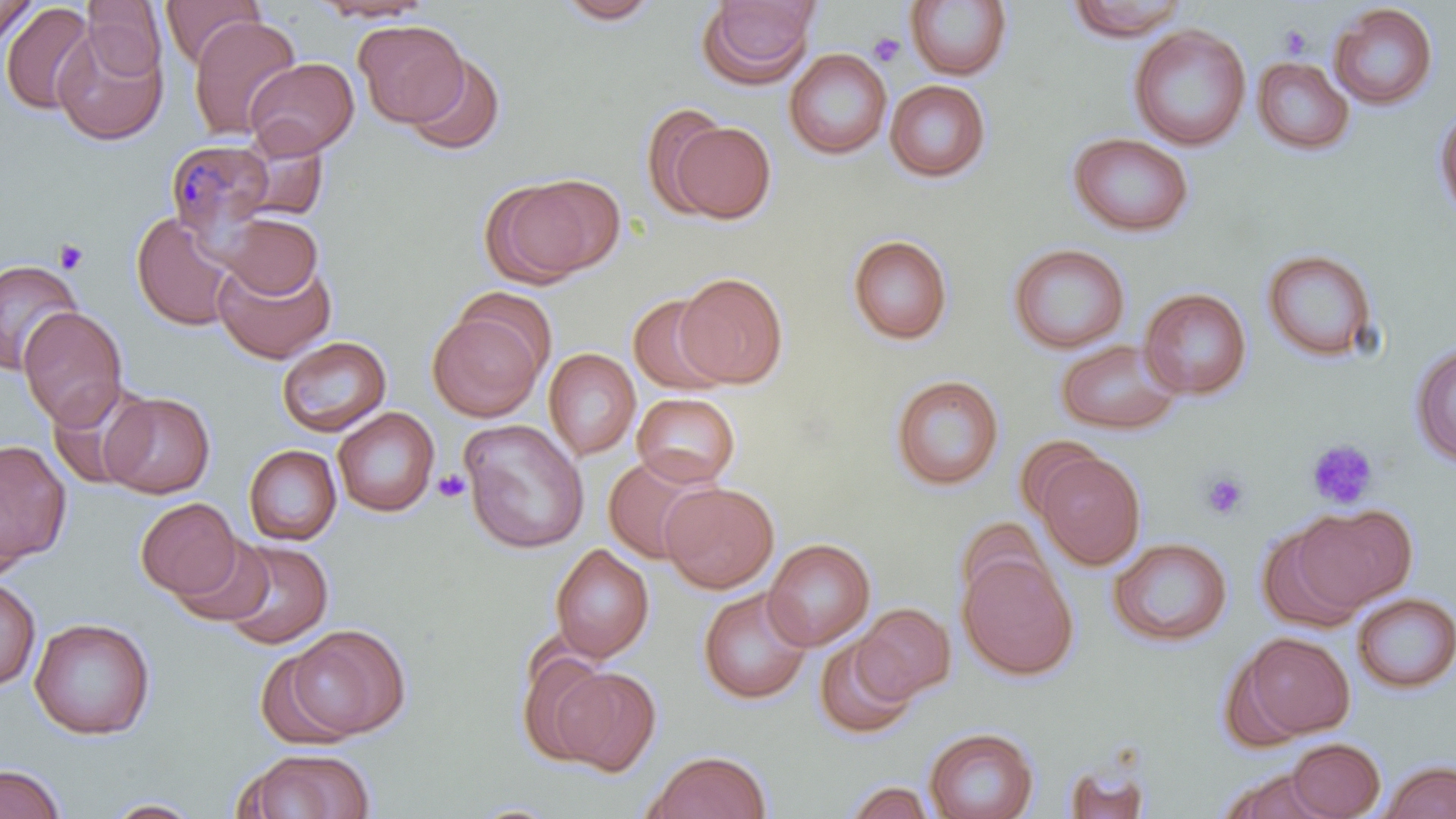
Summary:
  - Coordinate format: approximate bounding boxes as (x1,y1)-(x2,y2) corner pairs in pixels
  - Uninfected red blood cell locations: (82,0)-(167,78), (160,0)-(265,69), (308,0)-(436,23), (554,0)-(663,25), (1065,0)-(1191,42), (0,1)-(37,49), (696,1)-(821,89), (904,1)-(1013,81), (0,3)-(97,115), (1328,3)-(1439,111), (188,15)-(301,140), (354,20)-(468,127), (52,23)-(168,146), (1128,24)-(1251,152), (784,48)-(892,160), (403,51)-(505,156), (245,57)-(360,158), (1252,57)-(1355,156), (885,80)-(992,183), (1433,101)-(1456,225), (641,104)-(732,217), (664,120)-(777,223), (232,131)-(330,223), (1067,132)-(1194,237), (483,175)-(616,285), (131,211)-(239,332), (218,212)-(323,299), (846,234)-(953,345), (1007,242)-(1131,354), (1261,248)-(1380,364), (212,255)-(336,364), (0,259)-(83,374), (675,272)-(788,388), (454,286)-(558,377), (1139,287)-(1252,400), (627,295)-(731,396), (18,306)-(128,429), (428,309)-(544,421), (276,335)-(392,436), (1055,339)-(1183,435), (1408,340)-(1456,467), (543,348)-(641,460), (890,374)-(1005,491), (47,378)-(156,491), (100,391)-(216,498), (632,392)-(741,488), (332,407)-(439,517), (459,419)-(590,554), (1017,434)-(1104,522), (0,440)-(72,568), (243,444)-(342,546), (1035,451)-(1145,570), (602,454)-(718,564), (660,481)-(779,593), (135,497)-(242,600), (1291,503)-(1418,612), (955,517)-(1051,609), (1256,526)-(1366,633), (171,533)-(275,626), (1108,536)-(1233,647), (221,538)-(334,649), (763,538)-(876,651), (550,543)-(654,663), (957,553)-(1078,680), (0,576)-(41,691), (697,587)-(813,705), (1352,592)-(1456,694), (853,603)-(955,702), (29,617)-(156,740), (285,623)-(410,740), (1236,632)-(1356,740), (814,636)-(919,741), (517,648)-(614,765), (253,649)-(356,748), (553,666)-(662,775), (924,727)-(1038,819), (1286,738)-(1385,818), (236,748)-(377,818), (644,750)-(772,819), (1380,760)-(1456,818), (1,763)-(66,819), (1062,763)-(1150,819), (1220,768)-(1334,818), (843,780)-(937,819), (99,797)-(206,818)
  - Platelet locations: (1278,23)-(1313,59), (868,32)-(907,68), (54,239)-(89,274), (1306,439)-(1378,509), (432,468)-(471,503), (1201,472)-(1250,520)
  - Plasmodium malariae-infected red blood cell locations: (165,138)-(278,243)
  - Slide-level diagnosis: Plasmodium malariae
  - Stain: May-Grünwald-Giemsa
  - Field of view: single
  - Preparation: thin blood film
  - Image size: 1456×819 pixels
  - Modality: light microscopy
  - Magnification: 1000x